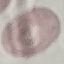

Summary:
  - Malaria status: uninfected
  - Stain: Giemsa
  - Preparation: thin smear
  - Capture: smartphone through the microscope eyepiece
  - Image type: cell patch, automatically extracted from a larger field of view and resized to 64 × 64 pixels